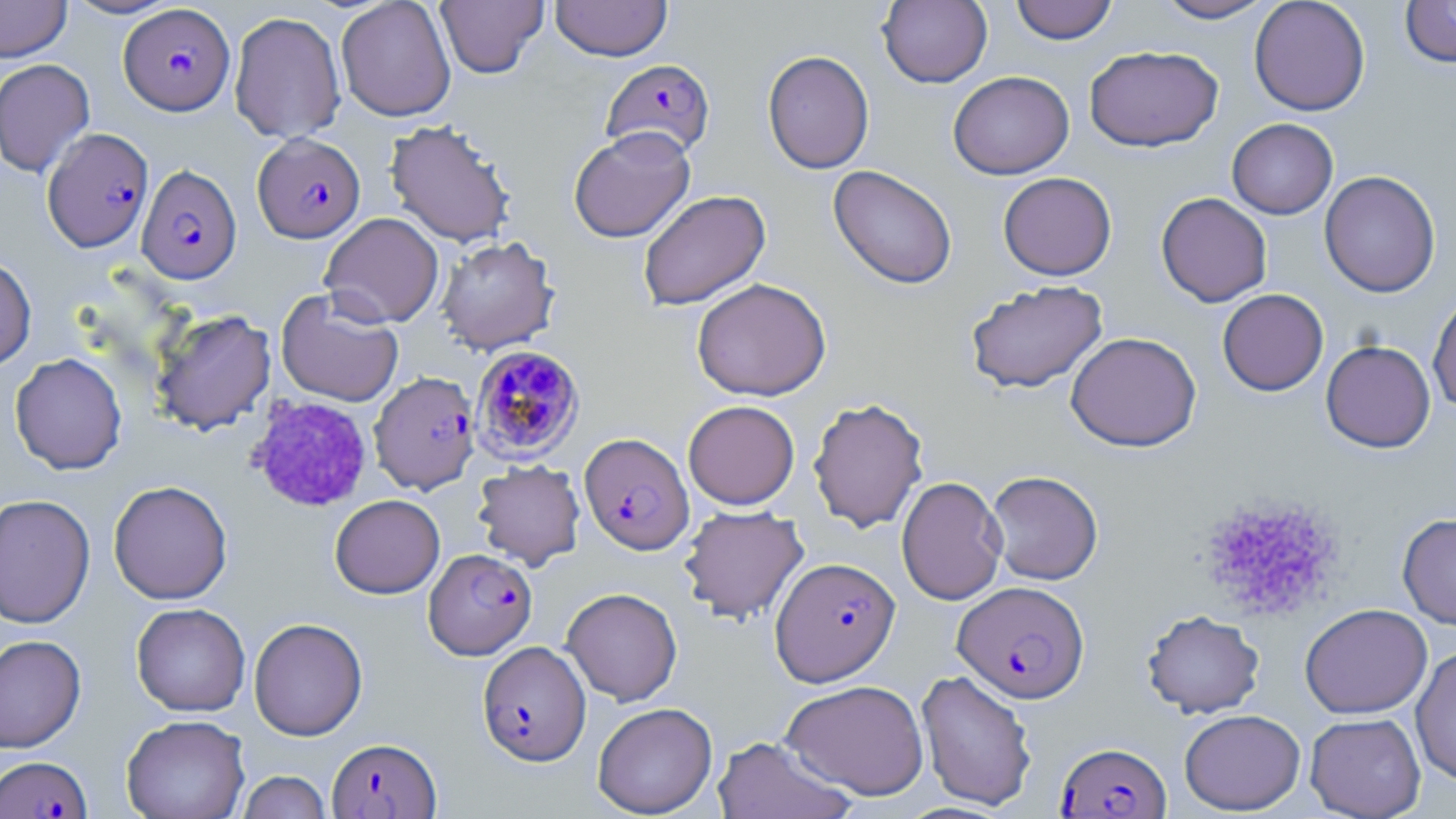

Summary:
  - Coordinate format: approximate bounding boxes as [x1, y1, x2, y2] in pixels
  - Plasmodium falciparum-infected red blood cell locations: [119, 3, 235, 115], [601, 58, 715, 159], [42, 127, 154, 252], [252, 133, 365, 243], [136, 164, 242, 284], [470, 344, 584, 462], [370, 371, 481, 494], [579, 432, 694, 555], [424, 548, 536, 660], [770, 556, 900, 686], [952, 580, 1089, 703], [477, 641, 591, 766], [327, 737, 440, 818], [1057, 741, 1171, 818], [0, 756, 92, 818]
  - Uninfected red blood cell locations (subset): [0, 0, 72, 62], [62, 0, 181, 20], [335, 0, 456, 121], [435, 0, 548, 78], [550, 0, 672, 61], [878, 0, 992, 88], [1010, 0, 1118, 44], [1153, 0, 1276, 23], [1249, 0, 1370, 116], [1400, 0, 1456, 68], [229, 11, 346, 144], [1084, 45, 1223, 152], [762, 50, 875, 174], [0, 58, 95, 178], [948, 71, 1074, 179], [1227, 118, 1338, 219], [385, 119, 517, 247], [568, 126, 696, 243], [828, 165, 957, 289], [1319, 170, 1441, 297], [998, 171, 1117, 280], [637, 190, 771, 311], [1156, 192, 1272, 307], [319, 212, 445, 328], [436, 236, 560, 355], [0, 256, 37, 370], [691, 278, 831, 401], [964, 280, 1108, 394], [276, 289, 404, 407], [1217, 289, 1328, 396], [1428, 291, 1456, 412], [150, 309, 276, 434], [1065, 332, 1202, 452], [1321, 340, 1436, 453], [10, 352, 128, 475], [808, 397, 929, 533], [683, 400, 800, 509], [472, 459, 586, 570], [985, 469, 1104, 585], [896, 476, 1007, 605], [108, 480, 233, 604], [0, 494, 95, 628], [330, 494, 445, 598], [679, 505, 808, 624], [1397, 512, 1456, 630], [561, 587, 683, 706], [131, 603, 250, 716], [1299, 603, 1432, 719], [1142, 609, 1265, 718], [249, 617, 368, 740], [0, 634, 87, 752], [1410, 645, 1456, 786], [916, 669, 1037, 811], [781, 679, 929, 800], [592, 702, 717, 818], [1179, 709, 1305, 814], [1305, 713, 1426, 819], [121, 714, 250, 819], [713, 736, 857, 819], [237, 770, 332, 819]
  - Platelet locations (subset): [1198, 495, 1344, 620]
  - Slide-level diagnosis: Plasmodium falciparum
  - Preparation: thin blood film
  - Field of view: one of a larger specimen
  - Modality: light microscopy
  - Stain: May-Grünwald-Giemsa
  - Image size: 1456×819 pixels
  - Magnification: 1000x